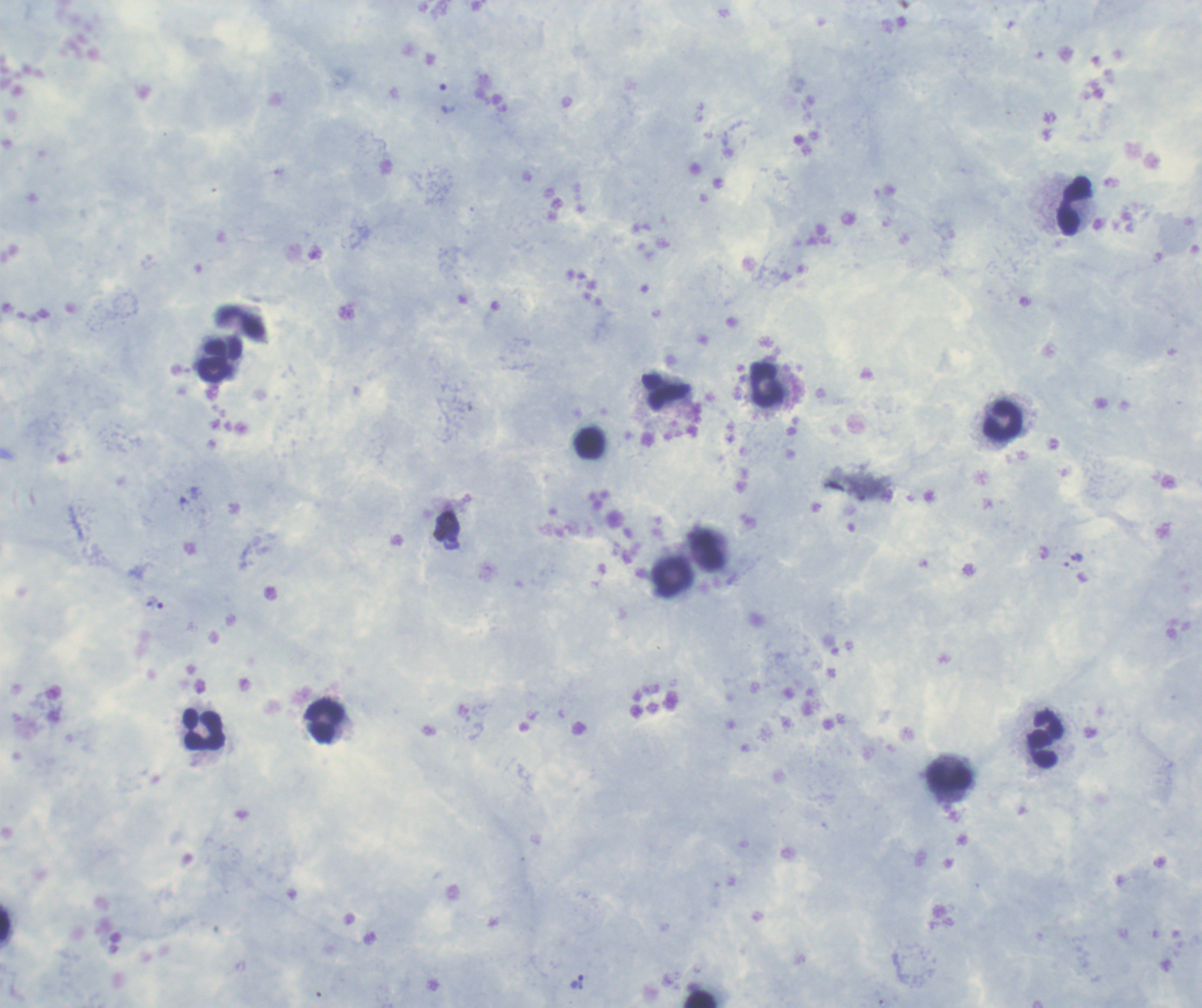 Coloration quality: good. Romanowsky stain. Single field of view. Thick smear of blood. Image is 1202×1008 pixels.